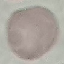
{
  "malaria_status": "uninfected",
  "image_type": "cell patch, automatically extracted from a larger field of view and resized to 64 × 64 pixels",
  "preparation": "thin blood smear",
  "stain": "Giemsa",
  "capture": "smartphone through the microscope eyepiece"
}